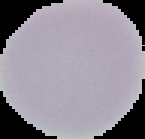

Summary:
  - Preparation: thin blood smear
  - Image type: cell region segmented out of the field of view; surrounding area masked to black
  - Result: no Plasmodium parasites detected
  - Image size: 145×139 pixels